Point out each malaria parasite and each leukocyte.
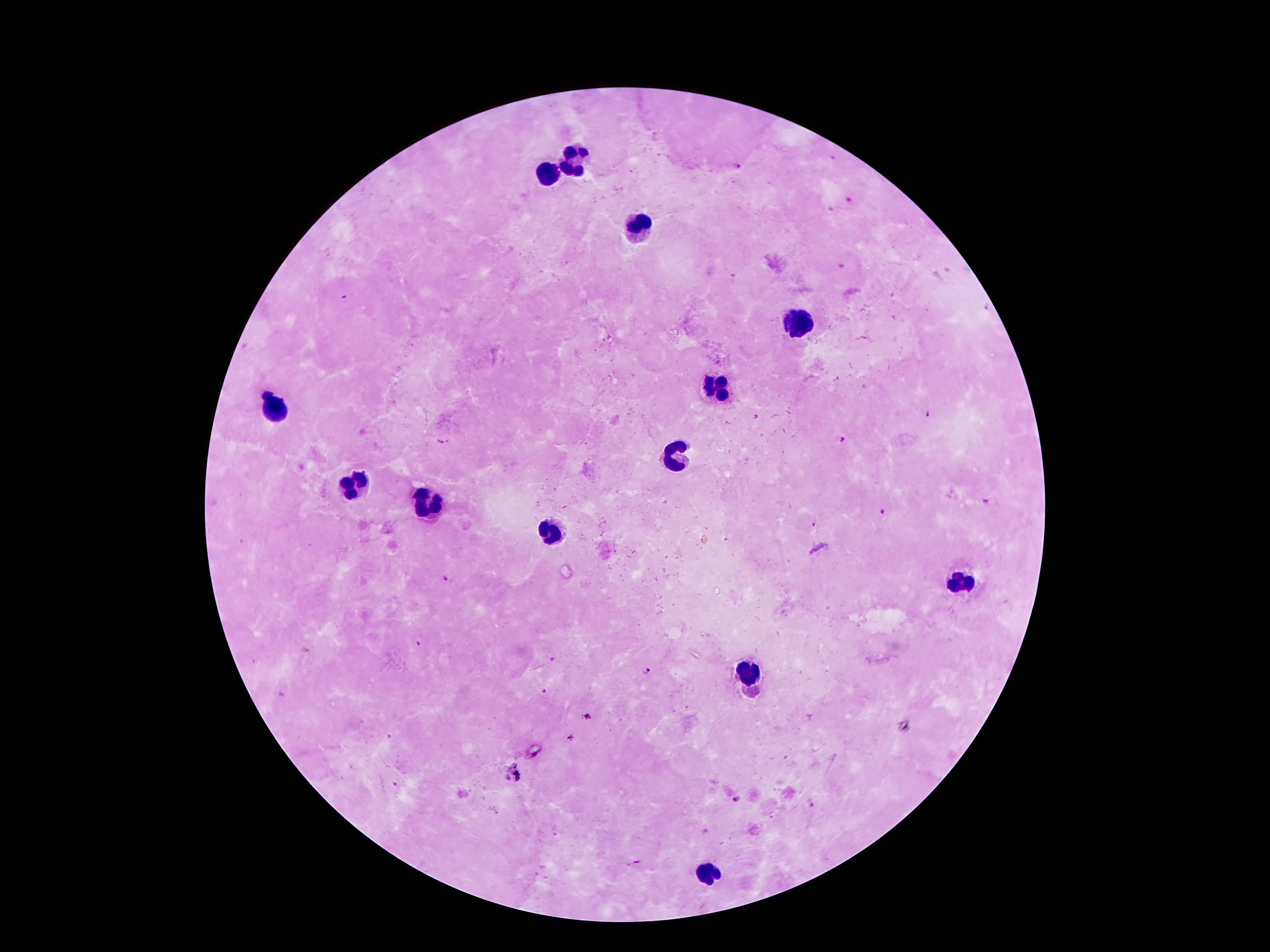
Approximate centers as [x, y] in pixels.
Malaria parasites: [739, 167], [849, 201], [842, 266], [345, 297], [985, 306], [926, 414], [754, 417], [842, 438], [987, 502], [878, 511], [444, 578], [418, 644], [552, 658], [647, 673], [543, 691], [587, 717], [571, 737], [394, 785], [733, 798].
Leukocytes: [575, 162], [549, 172], [640, 225], [794, 325], [716, 388], [269, 410], [677, 456], [353, 486], [423, 507], [551, 536], [956, 586], [748, 674], [708, 874].

Summary:
  - Capture: smartphone camera through the microscope eyepiece
  - Field of view: one from this slide
  - Preparation: thick blood film
  - Image size: 1270×952 pixels
  - Magnification: 100x
  - Patient malaria status: positive for Plasmodium falciparum
  - Stain: Giemsa